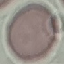

malaria status = uninfected
stain = Giemsa
image type = automatically extracted cell patch, resized to 64 × 64 pixels
capture = smartphone through the microscope eyepiece
preparation = thin blood film